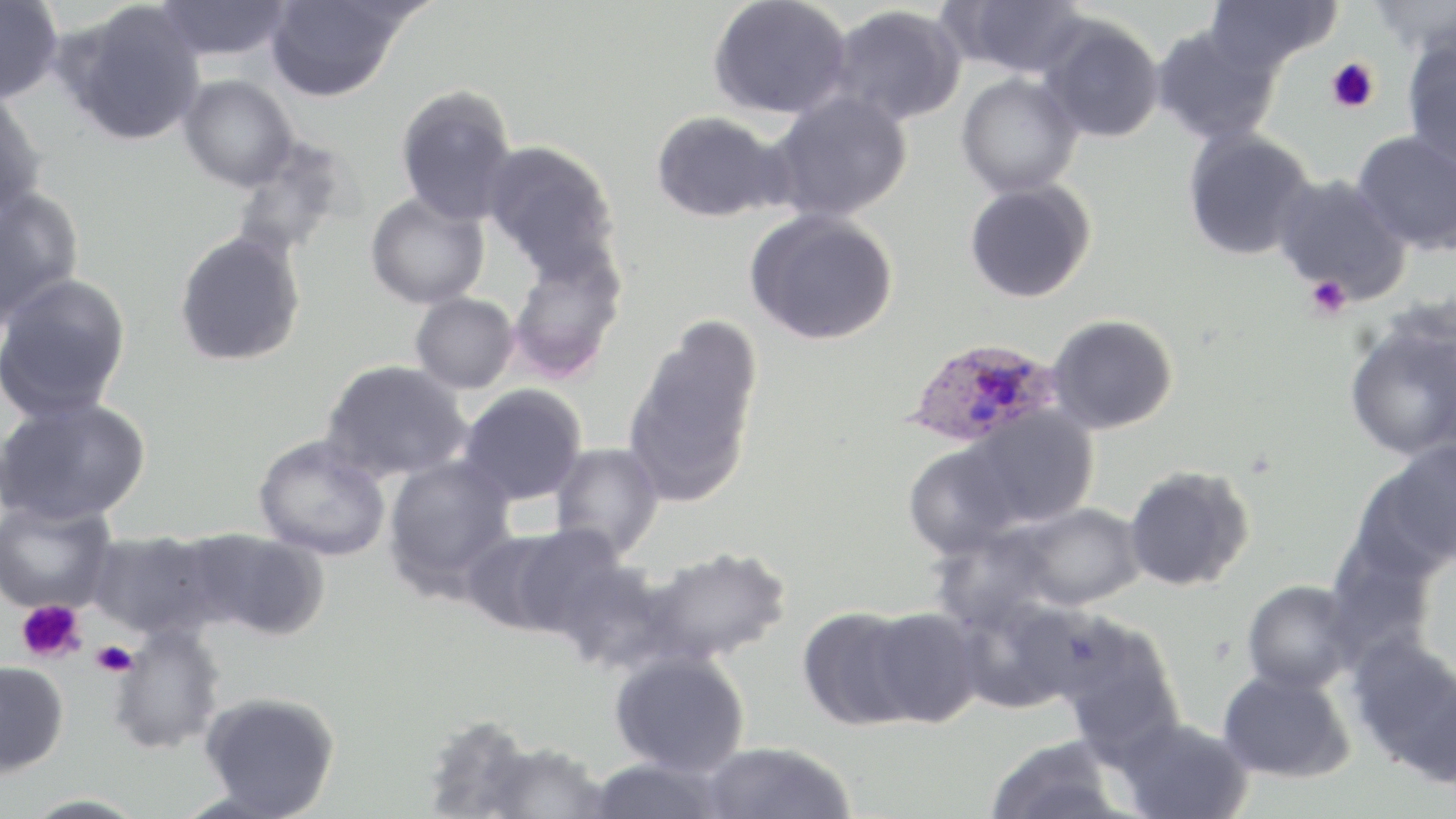
{
  "slide_level_diagnosis": "Plasmodium ovale",
  "magnification": "1000x",
  "field_of_view": "one of a larger specimen",
  "plasmodium_ovale_infected_red_blood_cell_locations": "approximate bounding boxes as [x1, y1, x2, y2] in pixels: [904, 337, 1061, 450]",
  "uninfected_red_blood_cell_locations": "approximate bounding boxes as [x1, y1, x2, y2] in pixels: [153, 0, 295, 62], [707, 0, 853, 120], [942, 0, 1090, 79], [1204, 0, 1343, 76], [1367, 0, 1455, 59], [0, 1, 64, 104], [57, 1, 207, 148], [265, 1, 412, 102], [828, 4, 967, 127], [1037, 15, 1165, 143], [1150, 24, 1284, 146], [1401, 34, 1456, 171], [956, 72, 1083, 198], [177, 74, 299, 192], [394, 84, 519, 225], [0, 87, 48, 222], [766, 90, 913, 222], [650, 109, 793, 223], [1181, 127, 1319, 261], [1351, 129, 1456, 255], [230, 138, 359, 262], [482, 138, 620, 277], [1270, 173, 1411, 303], [963, 179, 1096, 304], [0, 187, 85, 329], [365, 190, 491, 310], [744, 208, 899, 346], [173, 229, 306, 368], [505, 245, 628, 383], [0, 272, 132, 422], [409, 292, 520, 395], [1047, 313, 1178, 435], [622, 319, 762, 507], [1344, 322, 1455, 462], [320, 360, 473, 484], [458, 384, 587, 506], [1, 395, 151, 526], [961, 405, 1099, 529], [252, 434, 392, 562], [1363, 440, 1456, 572], [548, 442, 665, 560], [903, 443, 1023, 559], [383, 454, 518, 595], [1123, 465, 1255, 592], [0, 497, 118, 615], [1004, 501, 1147, 611], [461, 525, 613, 638], [183, 528, 330, 641], [86, 530, 225, 640], [639, 546, 792, 668], [550, 555, 677, 674], [1242, 578, 1361, 693], [959, 599, 1110, 712], [796, 606, 923, 731], [866, 607, 984, 727], [1056, 621, 1184, 758], [107, 623, 227, 756], [1351, 637, 1456, 783], [609, 649, 751, 777], [0, 660, 69, 777], [1217, 668, 1354, 783], [199, 691, 342, 818], [421, 715, 543, 818], [1117, 717, 1253, 819], [984, 735, 1125, 819], [477, 739, 612, 819], [699, 741, 857, 819], [587, 756, 732, 818], [19, 793, 151, 819]",
  "image_size": "1456×819 pixels",
  "preparation": "thin blood film",
  "modality": "light microscopy",
  "platelet_locations": "approximate bounding boxes as [x1, y1, x2, y2] in pixels: [1326, 57, 1381, 114], [1305, 276, 1352, 319], [16, 600, 85, 663], [90, 640, 138, 677]",
  "stain": "May-Grünwald-Giemsa"
}